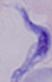

{
  "modality": "micrograph",
  "identification": "trypanosome",
  "magnification": "1000x"
}